Outline each uninfected red blood cell.
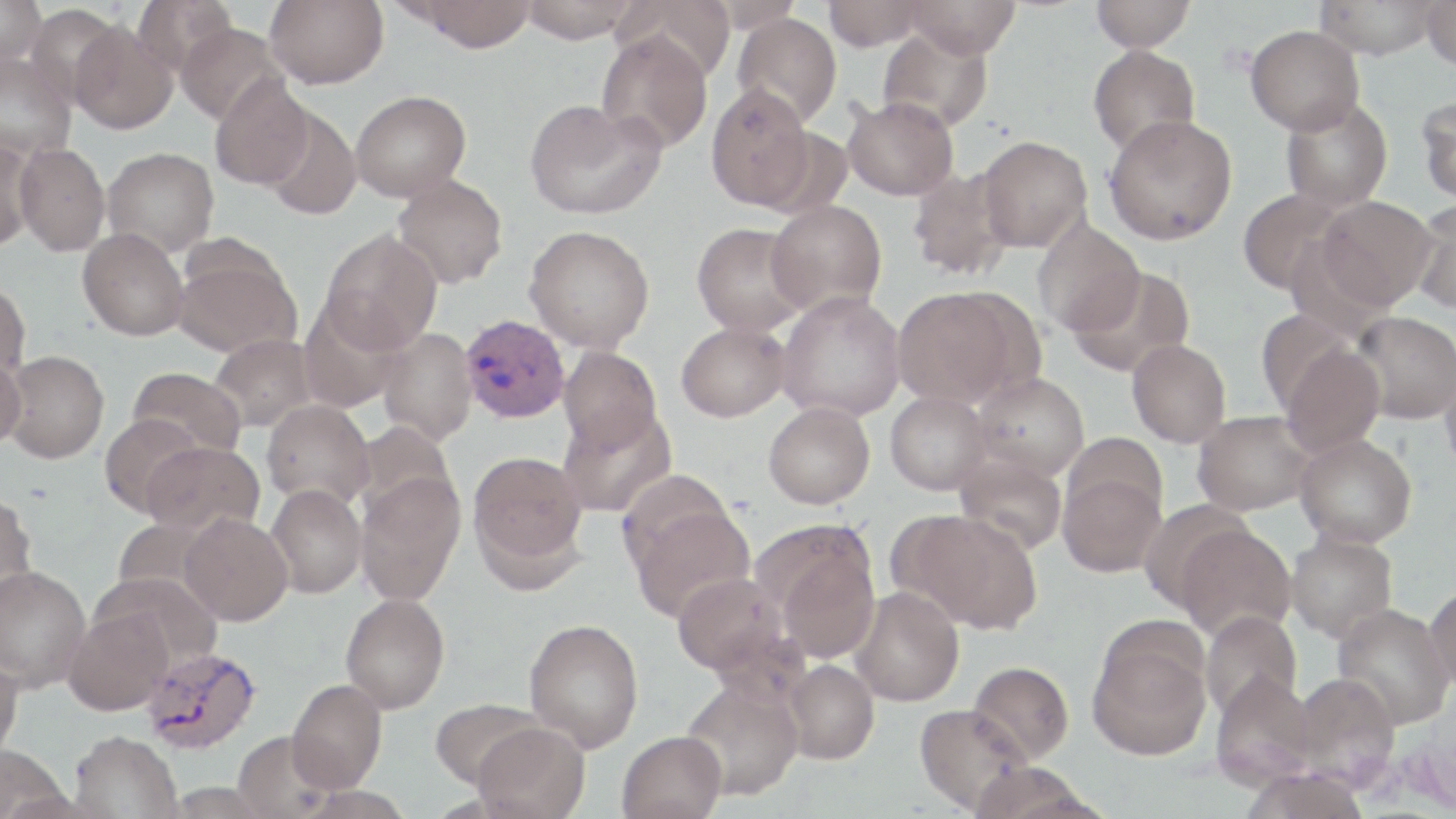

Approximate bounding boxes as [x1, y1, x2, y2] in pixels.
Uninfected red blood cells: [0, 0, 46, 66], [133, 0, 236, 79], [265, 0, 388, 89], [407, 0, 538, 52], [518, 0, 642, 43], [611, 0, 735, 83], [822, 0, 927, 50], [904, 0, 1021, 58], [1090, 0, 1196, 51], [1313, 0, 1444, 59], [1421, 0, 1456, 70], [700, 1, 805, 32], [25, 3, 123, 107], [732, 13, 842, 129], [70, 21, 177, 133], [175, 22, 287, 125], [1245, 24, 1364, 135], [877, 27, 993, 133], [595, 30, 712, 153], [1088, 45, 1200, 156], [0, 52, 76, 160], [209, 75, 316, 190], [706, 84, 815, 210], [351, 90, 471, 202], [1417, 94, 1456, 204], [843, 97, 958, 201], [524, 98, 665, 219], [1279, 98, 1393, 211], [261, 106, 362, 220], [1103, 114, 1237, 245], [976, 135, 1092, 252], [0, 139, 38, 252], [14, 142, 110, 256], [102, 146, 219, 257], [906, 168, 1014, 281], [392, 175, 508, 289], [1238, 188, 1351, 295], [1316, 196, 1436, 310], [767, 199, 887, 315], [1411, 200, 1456, 314], [1032, 219, 1146, 337], [692, 223, 809, 336], [524, 225, 655, 352], [77, 228, 189, 341], [320, 228, 442, 354], [172, 247, 302, 358], [1068, 265, 1195, 378], [0, 280, 31, 382], [892, 287, 1031, 409], [777, 291, 906, 422], [298, 299, 407, 413], [1255, 308, 1358, 416], [1352, 310, 1456, 424], [677, 322, 791, 422], [377, 328, 477, 445], [208, 334, 319, 433], [1127, 339, 1231, 448], [1279, 342, 1385, 457], [558, 345, 662, 451], [0, 350, 27, 449], [3, 350, 109, 463], [1440, 363, 1456, 478], [127, 366, 247, 460], [971, 373, 1089, 480], [885, 391, 992, 495], [262, 399, 375, 508], [763, 402, 875, 508], [558, 405, 677, 518], [1193, 410, 1316, 515], [98, 413, 206, 518], [352, 420, 457, 523], [1064, 432, 1168, 527], [1295, 433, 1417, 547], [142, 440, 264, 537], [468, 451, 588, 576], [954, 451, 1068, 555], [617, 468, 739, 578], [1058, 470, 1165, 578], [355, 473, 466, 605], [266, 483, 367, 598], [0, 492, 38, 604], [1138, 498, 1254, 612], [627, 502, 756, 623], [900, 510, 1042, 634], [180, 513, 292, 625], [1175, 523, 1297, 640], [1286, 530, 1398, 642], [766, 532, 880, 663], [0, 565, 91, 691], [671, 571, 789, 677], [1425, 582, 1456, 696], [850, 586, 964, 707], [340, 592, 450, 714], [1332, 603, 1454, 730], [63, 609, 173, 716], [1200, 611, 1302, 719], [524, 618, 644, 753], [1088, 630, 1212, 761], [0, 654, 23, 762], [783, 659, 879, 764], [968, 661, 1074, 764], [1210, 672, 1317, 791], [1291, 672, 1400, 789], [678, 678, 803, 801], [287, 680, 387, 792], [430, 698, 546, 791], [914, 702, 1032, 814], [473, 721, 590, 818], [69, 730, 183, 819], [233, 730, 335, 818], [617, 730, 727, 819], [0, 745, 71, 819], [1239, 766, 1371, 819].

Summary:
  - Plasmodium vivax-infected red blood cell locations: [460, 314, 570, 423], [140, 645, 261, 754]
  - Slide-level diagnosis: Plasmodium vivax
  - Modality: light microscopy
  - Stain: May-Grünwald-Giemsa
  - Preparation: thin blood film
  - Image size: 1456×819 pixels
  - Magnification: 1000x
  - Field of view: one of a larger specimen